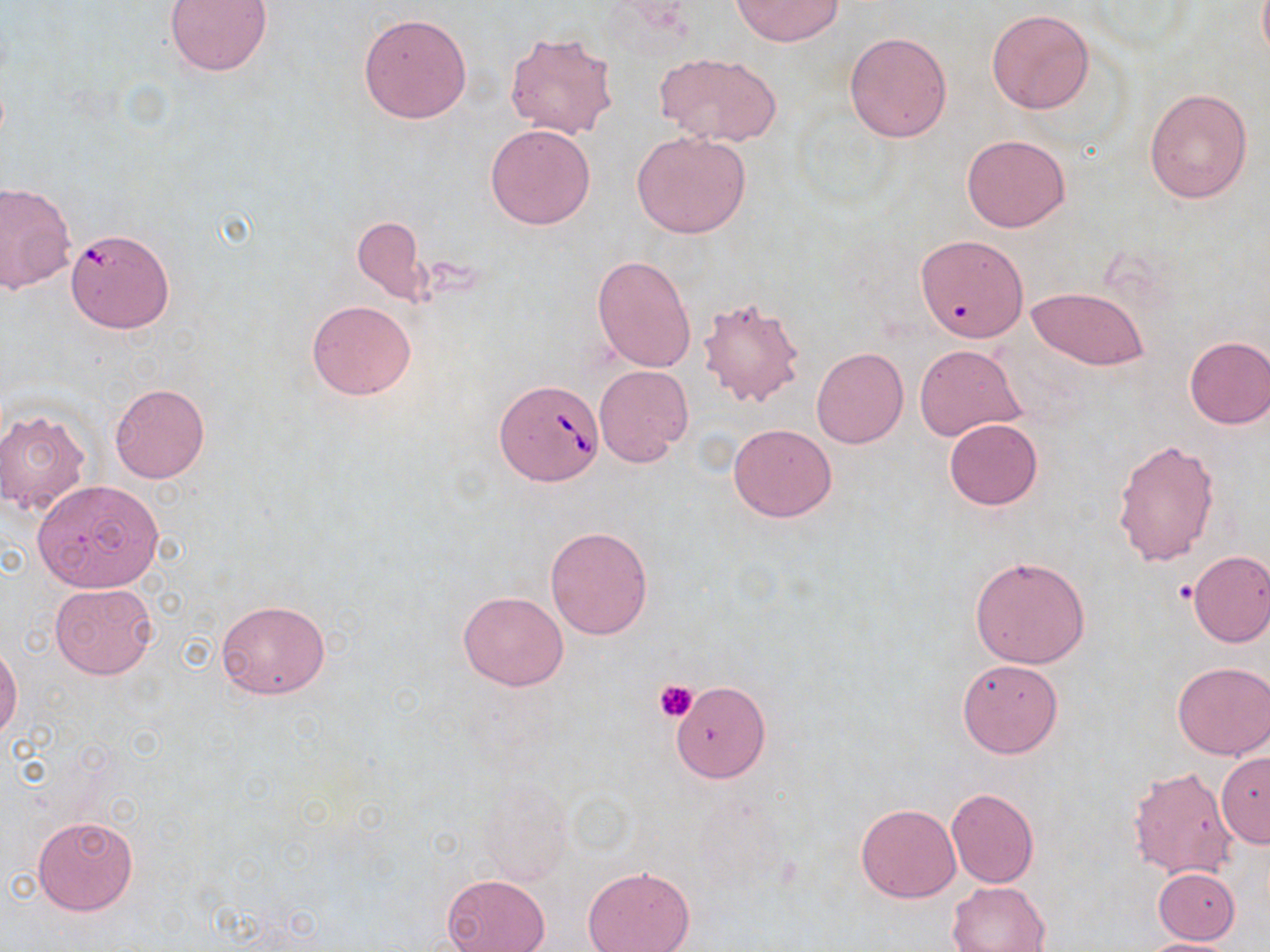

slide-level diagnosis = Babesia divergens
uninfected red blood cell locations = approximate bounding boxes as named x1/y1/x2/y2 corners in pixels: (x1=165, y1=0, x2=272, y2=76), (x1=731, y1=0, x2=842, y2=46), (x1=987, y1=9, x2=1095, y2=114), (x1=358, y1=12, x2=473, y2=124), (x1=504, y1=31, x2=619, y2=140), (x1=844, y1=31, x2=952, y2=143), (x1=655, y1=52, x2=783, y2=148), (x1=1145, y1=87, x2=1254, y2=204), (x1=486, y1=124, x2=595, y2=230), (x1=631, y1=130, x2=751, y2=238), (x1=962, y1=135, x2=1070, y2=233), (x1=0, y1=182, x2=77, y2=294), (x1=351, y1=213, x2=430, y2=304), (x1=919, y1=239, x2=1030, y2=346), (x1=591, y1=254, x2=696, y2=374), (x1=1026, y1=286, x2=1149, y2=371), (x1=695, y1=293, x2=808, y2=410), (x1=307, y1=300, x2=416, y2=399), (x1=1183, y1=335, x2=1270, y2=429), (x1=916, y1=344, x2=1027, y2=440), (x1=812, y1=347, x2=908, y2=448), (x1=594, y1=365, x2=693, y2=466), (x1=109, y1=383, x2=209, y2=483), (x1=0, y1=406, x2=91, y2=516), (x1=943, y1=418, x2=1044, y2=510), (x1=728, y1=423, x2=836, y2=521), (x1=1113, y1=438, x2=1221, y2=567), (x1=32, y1=479, x2=164, y2=592), (x1=544, y1=525, x2=653, y2=640), (x1=1186, y1=550, x2=1270, y2=647), (x1=970, y1=555, x2=1090, y2=669), (x1=50, y1=583, x2=157, y2=678), (x1=457, y1=589, x2=569, y2=690), (x1=214, y1=598, x2=331, y2=699), (x1=0, y1=643, x2=22, y2=744), (x1=957, y1=659, x2=1063, y2=757), (x1=1171, y1=661, x2=1270, y2=761), (x1=671, y1=681, x2=771, y2=782), (x1=1216, y1=753, x2=1269, y2=847), (x1=1126, y1=763, x2=1240, y2=879), (x1=946, y1=789, x2=1039, y2=887), (x1=855, y1=804, x2=961, y2=903), (x1=32, y1=815, x2=140, y2=916), (x1=582, y1=865, x2=695, y2=952), (x1=1152, y1=867, x2=1240, y2=943), (x1=441, y1=874, x2=550, y2=952), (x1=947, y1=880, x2=1050, y2=952), (x1=1133, y1=937, x2=1244, y2=952)
preparation = thin blood smear
modality = light microscopy
stain = May-Grünwald-Giemsa
image size = 1270×952 pixels
field of view = one of a larger specimen
Babesia divergens-infected red blood cell locations = approximate bounding boxes as named x1/y1/x2/y2 corners in pixels: (x1=67, y1=235, x2=178, y2=337), (x1=496, y1=380, x2=604, y2=485)
platelet locations = approximate bounding boxes as named x1/y1/x2/y2 corners in pixels: (x1=1172, y1=579, x2=1200, y2=605), (x1=653, y1=680, x2=699, y2=722)
magnification = 1000x